Name the cell type shown.
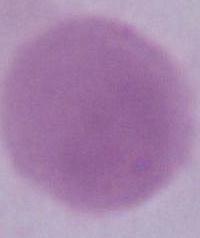
An erythrocyte.

1000x magnification. Photomicrograph.